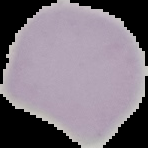

Image is 148×148 pixels. Cell region segmented out of the field of view; the surrounding area is masked to black. From a thin blood film. Malaria status: uninfected.